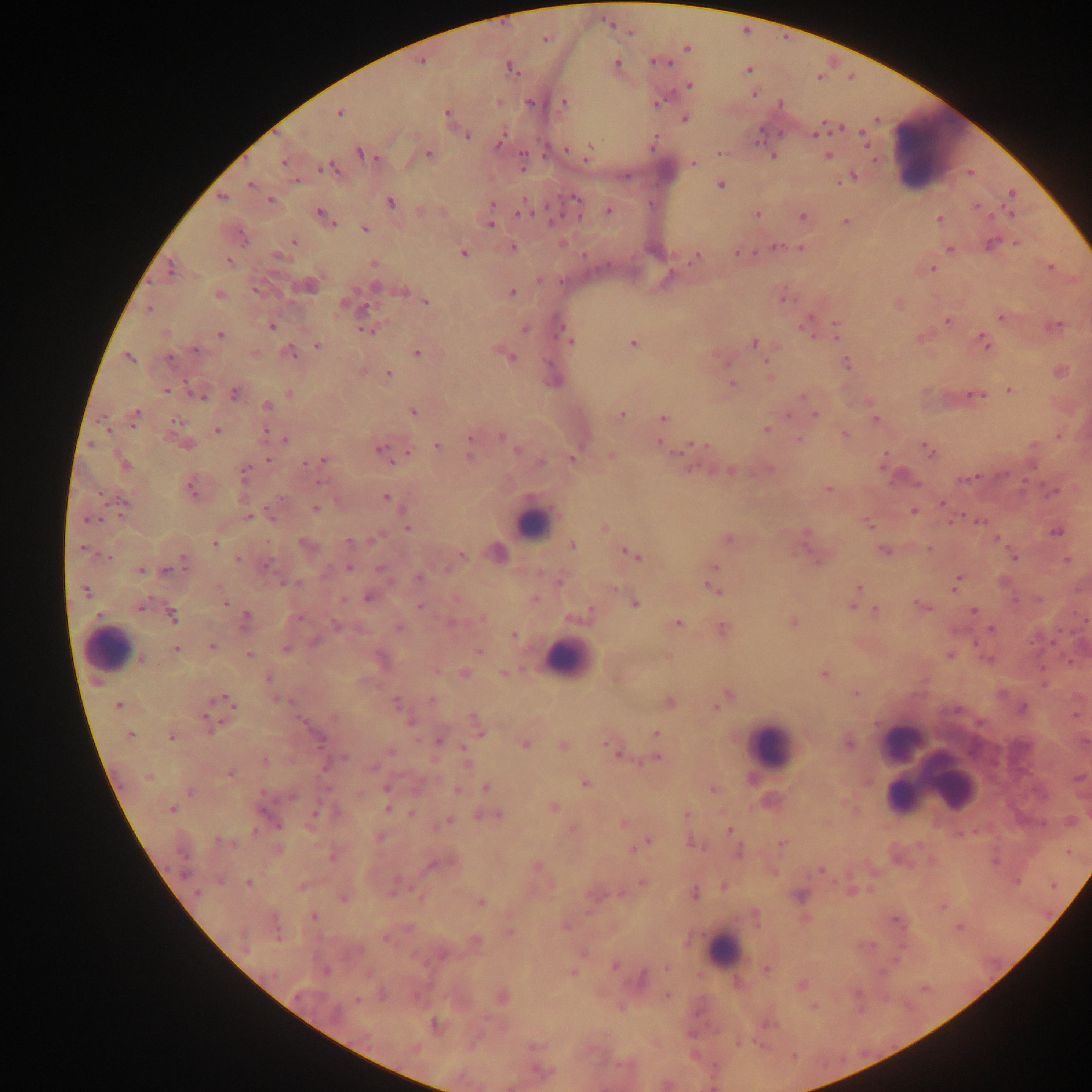
leukocyte locations = approximate centers as x y in pixels: 937 152; 532 523; 109 649; 569 658; 902 741; 769 745; 944 778; 913 783; 900 797; 723 951
Plasmodium parasite locations = approximate centers as x y in pixels: 629 32; 544 39; 686 48; 420 62; 616 62; 657 62; 511 68; 747 70; 690 85; 754 93; 498 102; 564 102; 530 103; 658 103; 781 103; 340 113; 447 113; 685 118; 818 131; 467 136; 864 138; 499 142; 653 143; 566 148; 720 152; 361 153; 428 154; 588 154; 773 156; 827 156; 283 163; 522 163; 693 164; 326 168; 852 177; 845 180; 297 181; 250 184; 721 185; 1012 193; 221 197; 576 198; 270 199; 390 202; 492 204; 976 205; 608 211; 523 212; 321 213; 756 214; 1009 214; 802 217; 940 219; 846 221; 332 223; 490 225; 365 228; 242 238; 294 242; 990 244; 1017 244; 775 245; 513 247; 801 248; 949 249; 463 253; 738 253; 279 256; 696 256; 228 261; 373 264; 1050 267; 170 269; 932 269; 375 286; 255 290; 403 291; 512 293; 218 294; 784 298; 426 302; 342 306; 148 308; 365 308; 1001 317; 948 321; 806 325; 272 326; 1056 326; 525 330; 835 330; 367 331; 219 335; 570 341; 984 341; 634 343; 754 343; 317 346; 195 349; 291 353; 417 354; 510 356; 129 357; 170 359; 847 364; 388 374; 732 383; 166 390; 1010 390; 234 393; 289 394; 198 395; 976 395; 801 396; 267 405; 413 412; 135 414; 621 415; 815 416; 663 417; 876 419; 176 421; 766 429; 217 430; 265 432; 844 435; 501 436; 470 437; 286 439; 798 439; 661 444; 696 444; 187 445; 437 445; 1034 445; 379 449; 928 449; 517 450; 407 453; 611 456; 470 457; 268 458; 324 459; 573 459; 541 462; 122 464; 305 464; 730 470; 769 470; 244 473; 964 478; 321 482; 190 488; 828 490; 1053 491; 386 498; 125 503; 943 504; 316 509; 913 512; 248 517; 272 518; 90 520; 980 521; 868 525; 407 527; 605 527; 1056 533; 376 538; 728 540; 997 540; 348 541; 304 543; 215 544; 572 546; 82 548; 929 548; 883 551; 461 554; 633 554; 107 557; 1014 557; 184 559; 238 559; 1067 560; 818 561; 268 565; 349 567; 713 567; 381 568; 447 568; 167 570; 141 571; 419 577; 560 581; 956 582; 293 583; 858 587; 713 589; 85 592; 344 599; 368 599; 535 599; 225 603; 634 604; 922 605; 419 606; 139 607; 852 607; 875 609; 974 611; 587 612; 173 616; 300 618; 246 619; 482 619; 792 622; 336 625; 676 625; 399 628; 991 628; 723 630; 514 635; 315 642; 211 647; 286 648; 176 649; 479 651; 249 655; 949 655; 141 659; 465 673; 504 673; 823 675; 268 677; 855 693; 729 695; 226 699; 431 700; 396 701; 670 703; 118 705; 716 707; 1022 708; 1074 716; 332 717; 475 720; 209 721; 408 722; 479 730; 655 732; 130 735; 171 738; 319 740; 438 741; 848 743; 525 744; 563 745; 610 747; 465 749; 390 751; 618 753; 344 757; 657 758; 265 760; 466 763; 374 767; 230 774; 148 777; 585 784; 486 787; 386 788; 713 790; 456 791; 263 792; 190 793; 292 797; 554 807; 171 809; 387 810; 316 813; 412 813; 686 814; 493 815; 448 821; 623 823; 276 824; 572 828; 729 830; 255 831; 218 840; 647 842; 692 844; 782 844; 738 852; 430 866; 537 866; 820 870; 247 882; 642 882; 302 887; 694 892; 197 893; 800 895; 344 898; 481 902; 314 916; 958 927; 566 928; 510 932; 278 934; 385 939; 614 966; 666 967; 325 970; 766 970; 572 973; 642 977; 801 984; 667 995; 502 997; 357 1001; 435 1023; 415 1048; 543 1071
field of view = single
preparation = thick blood smear
country = Ghana
image size = 1092×1092 pixels
capture = mobile-phone photograph through a microscope